Describe the morphology of the erythrocytes.
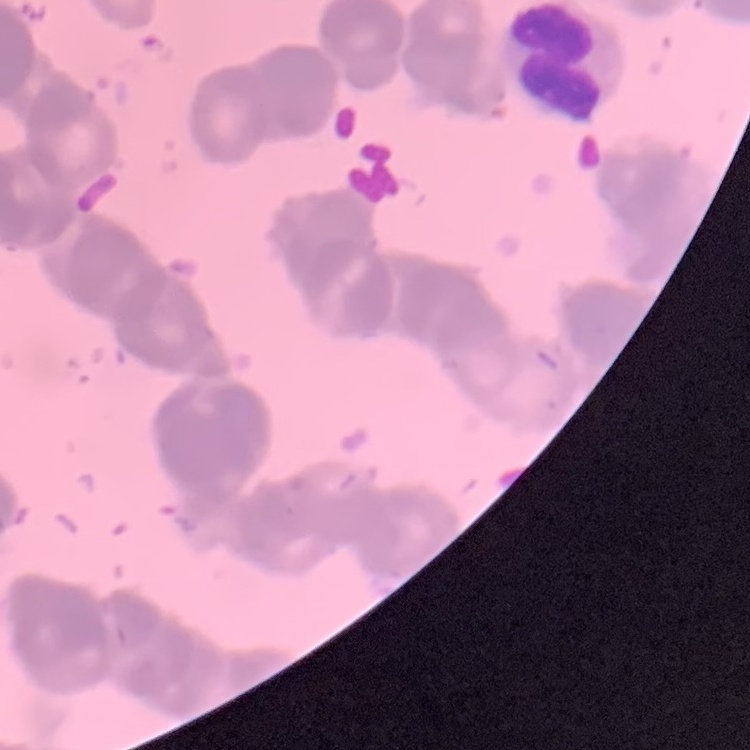

They show rouleaux formation.

preparation = thin blood smear
image type = one tile cut from a larger photomicrograph
stain = Field's or Giemsa